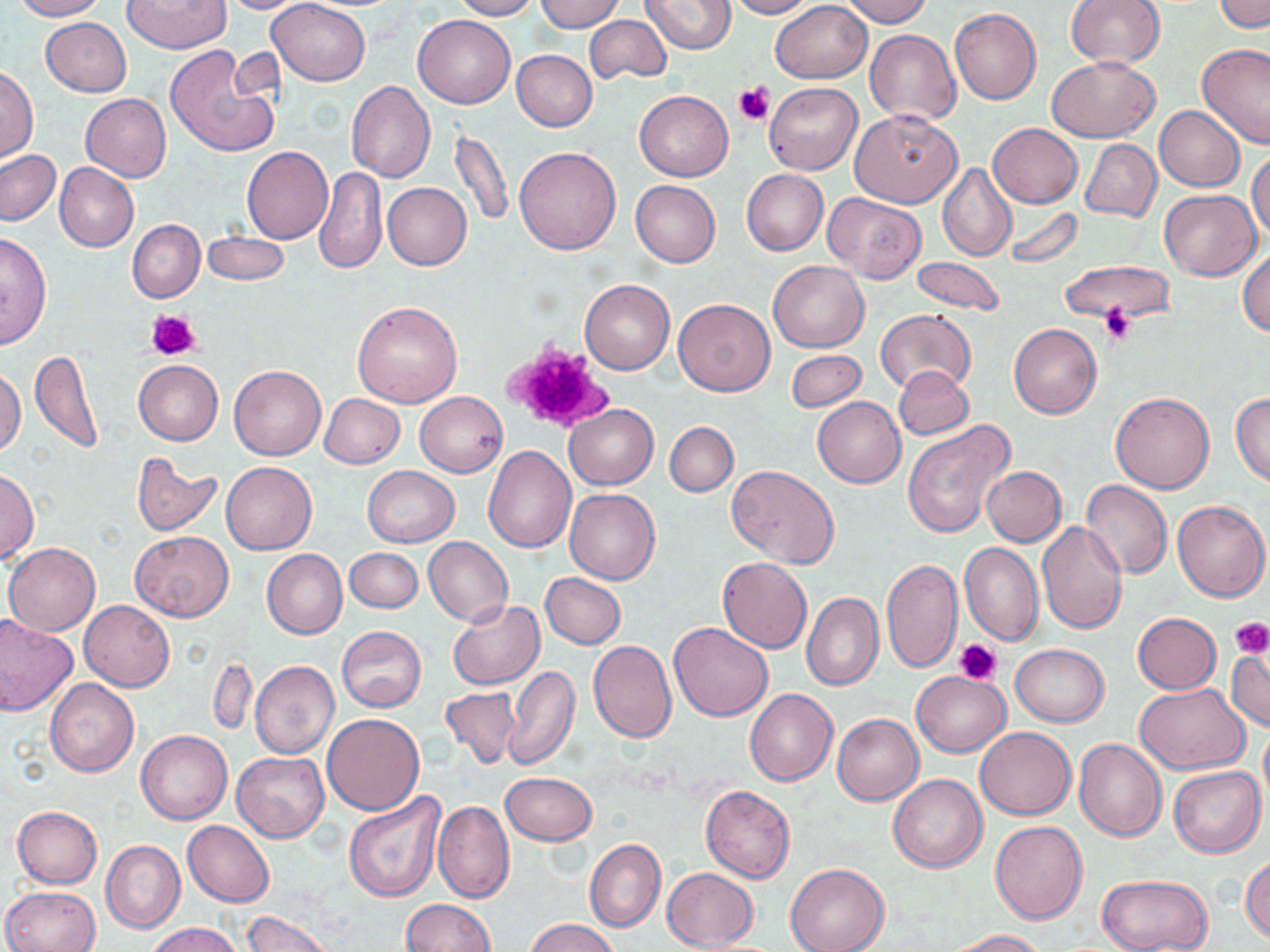
Approximate bounding boxes as (x1, y1, x2, y2) in pixels. Platelet locations: (733, 81, 773, 125), (1099, 306, 1136, 345), (147, 308, 201, 361), (503, 339, 615, 433), (1232, 618, 1270, 659), (955, 639, 1004, 684). Uninfected red blood cell locations: (10, 0, 107, 20), (217, 0, 310, 13), (266, 0, 371, 86), (451, 0, 540, 20), (535, 0, 625, 33), (640, 0, 737, 53), (723, 0, 814, 18), (840, 0, 932, 27), (1067, 0, 1165, 70), (122, 1, 231, 52), (770, 1, 871, 83), (1214, 1, 1269, 32), (950, 8, 1041, 104), (584, 12, 672, 85), (413, 14, 514, 108), (40, 17, 131, 96), (864, 28, 961, 126), (1198, 43, 1270, 149), (164, 45, 281, 158), (511, 51, 596, 132), (1047, 56, 1161, 143), (0, 66, 37, 163), (346, 81, 436, 183), (764, 82, 862, 174), (635, 90, 733, 182), (81, 94, 171, 181), (1154, 106, 1246, 192), (848, 109, 962, 208), (988, 123, 1082, 208), (448, 127, 513, 229), (1081, 139, 1161, 221), (243, 146, 333, 243), (513, 146, 621, 255), (1249, 148, 1270, 239), (1, 150, 61, 225), (55, 163, 139, 251), (938, 163, 1017, 261), (314, 166, 386, 275), (742, 169, 828, 255), (631, 180, 721, 267), (383, 182, 471, 270), (1160, 189, 1261, 280), (824, 192, 925, 283), (1002, 206, 1083, 269), (128, 219, 205, 303), (202, 232, 291, 286), (0, 233, 53, 349), (1237, 247, 1270, 337), (912, 256, 1004, 313), (1059, 260, 1172, 323), (770, 261, 869, 352), (579, 278, 675, 375), (673, 298, 775, 395), (352, 300, 462, 408), (876, 310, 976, 395), (1009, 324, 1101, 417), (28, 348, 104, 453), (786, 351, 865, 411), (134, 360, 223, 445), (228, 365, 326, 461), (893, 366, 973, 440), (0, 369, 25, 457), (1232, 391, 1270, 485), (415, 392, 508, 477), (1110, 392, 1214, 493), (320, 394, 404, 469), (813, 396, 906, 487), (563, 404, 658, 489), (902, 420, 1018, 540), (665, 421, 737, 497), (483, 445, 576, 553), (131, 455, 222, 535), (221, 462, 316, 554), (362, 465, 459, 547), (981, 465, 1066, 546), (727, 466, 840, 568), (1, 468, 38, 563), (1080, 481, 1174, 579), (563, 488, 660, 585), (1171, 500, 1269, 602), (1038, 521, 1128, 635), (132, 531, 233, 621), (424, 536, 513, 626), (4, 542, 101, 637), (960, 542, 1044, 645), (345, 547, 422, 613), (262, 549, 347, 638), (717, 557, 812, 653), (882, 558, 962, 673), (541, 574, 626, 648), (802, 591, 884, 691), (79, 599, 174, 691), (447, 601, 544, 690), (1132, 613, 1220, 694), (0, 615, 78, 717), (669, 622, 773, 721), (337, 626, 425, 711), (587, 640, 676, 743), (1009, 644, 1110, 727), (1227, 648, 1270, 731), (208, 656, 257, 735), (250, 661, 339, 759), (505, 666, 579, 771), (911, 670, 1009, 757), (46, 678, 138, 776), (1135, 682, 1251, 773), (439, 686, 523, 768), (745, 688, 837, 786), (833, 712, 923, 804), (323, 714, 425, 816), (974, 726, 1076, 820), (136, 729, 233, 825), (1074, 738, 1166, 841), (233, 752, 329, 843), (1169, 767, 1265, 857), (500, 772, 596, 845), (888, 774, 987, 873), (701, 785, 795, 883), (343, 790, 445, 904), (432, 800, 514, 904), (12, 806, 103, 888), (183, 820, 275, 907), (989, 820, 1088, 923), (584, 838, 665, 933), (101, 840, 186, 933), (1241, 855, 1270, 942), (785, 863, 891, 952), (662, 867, 758, 950), (1098, 874, 1211, 952), (2, 885, 100, 952), (402, 898, 495, 951), (244, 911, 333, 952), (526, 919, 617, 952), (146, 923, 243, 952), (944, 929, 1044, 951). Slide-level diagnosis: no evidence of blood parasites. Image is 1270×952 pixels. 1000x magnification. Light microscopy. One field of a larger specimen. May-Grünwald-Giemsa-stained preparation. Thin blood film.